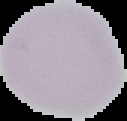 Image is 127×121 pixels. Cell region segmented out of the field of view; the surrounding area is masked to black. Malaria status: uninfected. From a thin blood film.